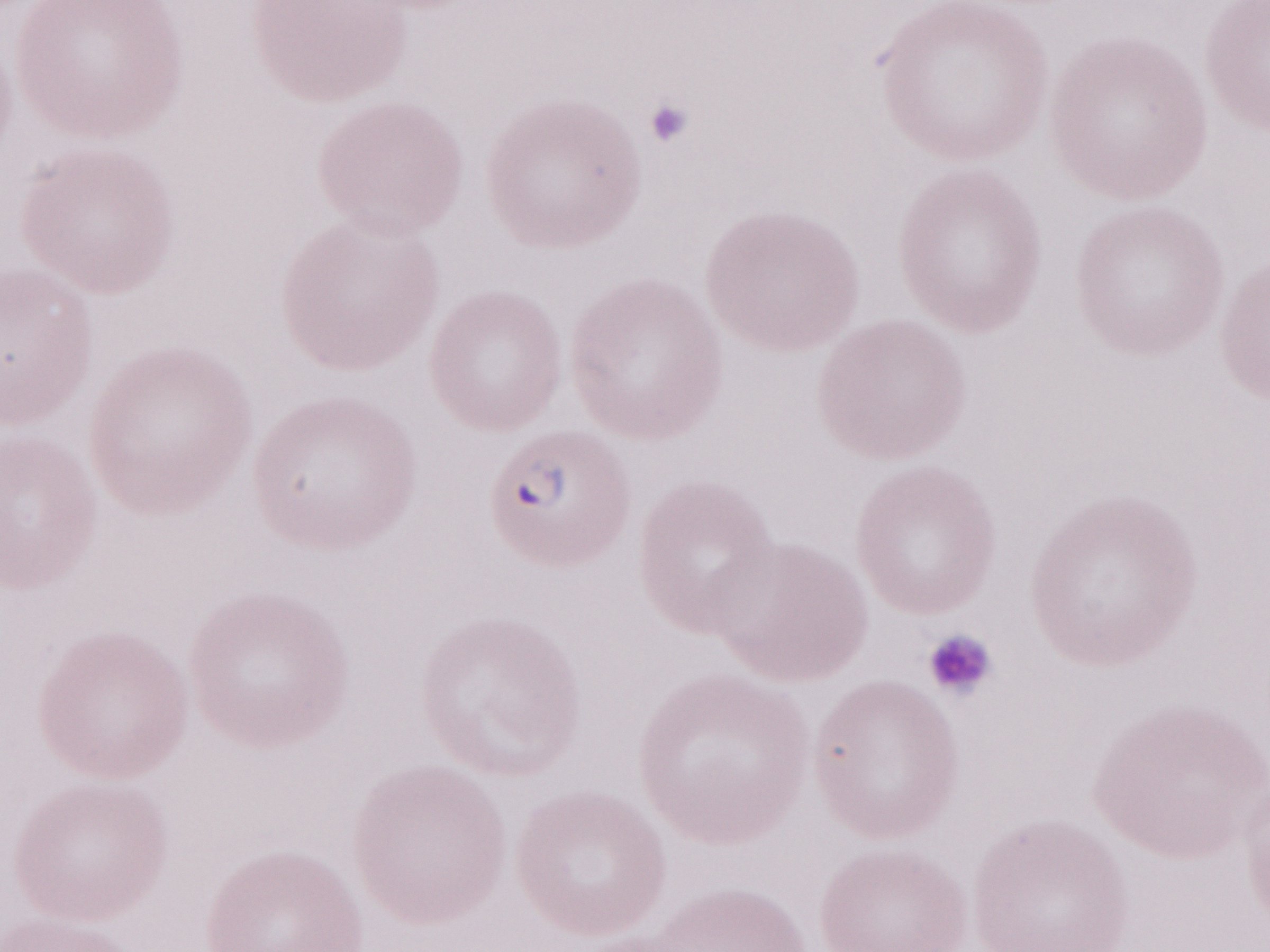

Olympus BX43 microscope and DP73 digital camera. 1,000x magnification. May-Grünwald-Giemsa-stained preparation. Malaria diagnosis (patient-level): positive. Thin peripheral-blood smear. Image is 1270×952 pixels. Single field of view.